Evaluate for malaria.
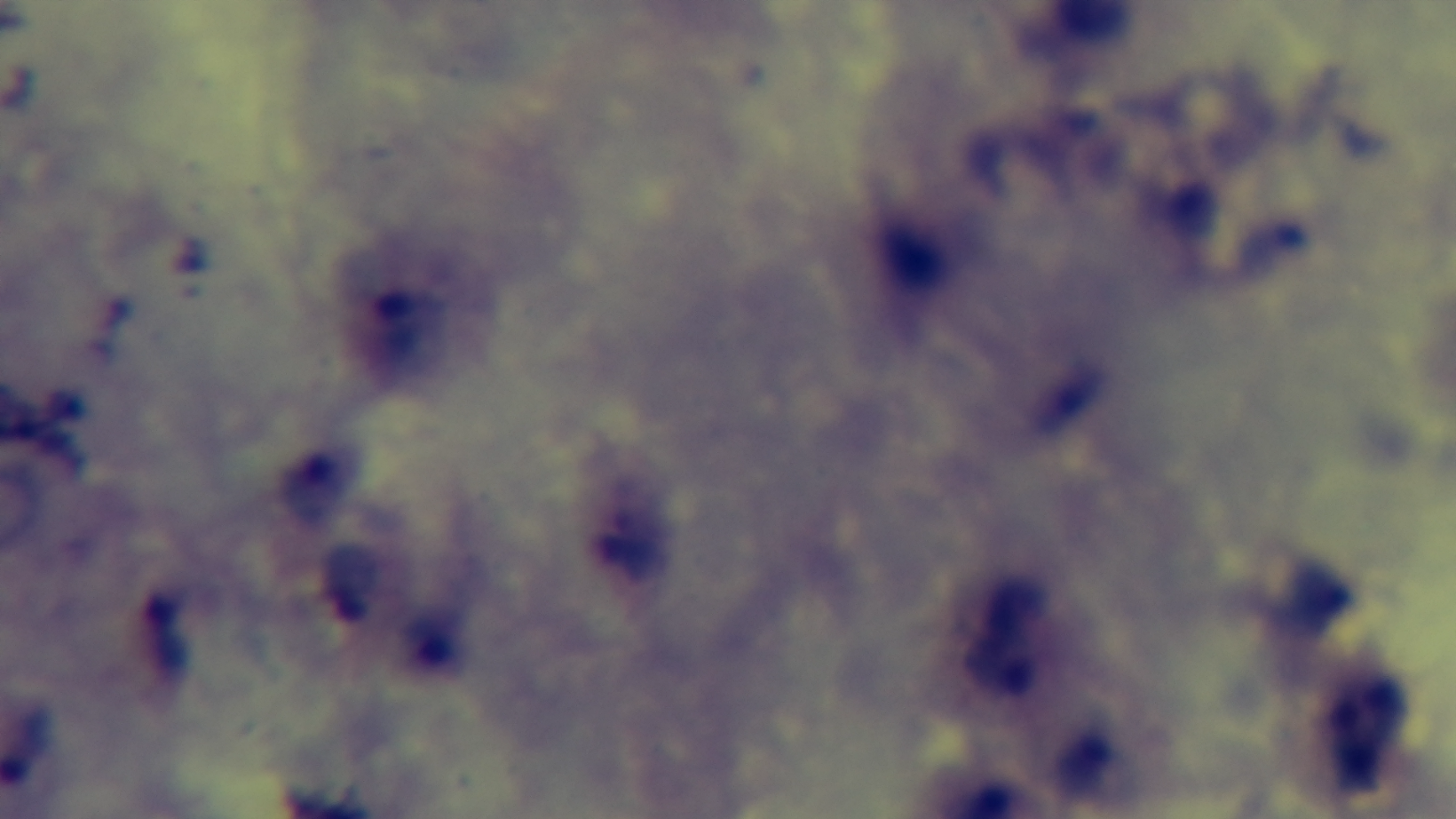
Infected.

Summary:
  - Preparation: thick
  - Modality: light microscopy
  - Objective: 100x oil immersion
  - Capture: mounted 4K digital camera
  - Stain: Giemsa
  - Field of view: single